Assess this cell for malaria.
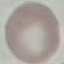
Uninfected.

Summary:
  - Preparation: thin smear
  - Stain: Giemsa
  - Capture: smartphone through the microscope eyepiece
  - Image type: automatically extracted cell patch, resized to 64 × 64 pixels